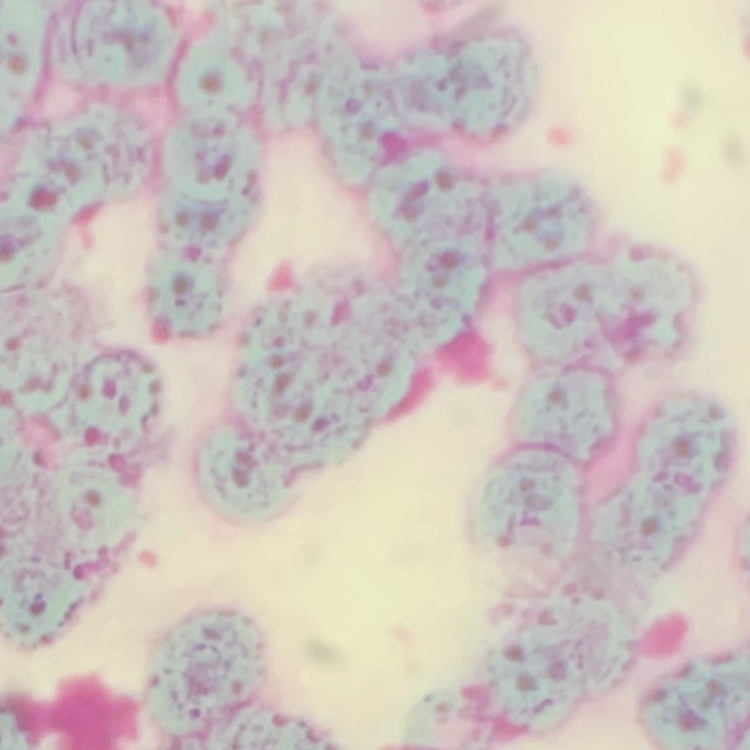 The red blood cells show rouleaux formation. One tile cut from a larger photomicrograph. Stained with either Field's or Giemsa. Thin blood film.